State the preparation type.
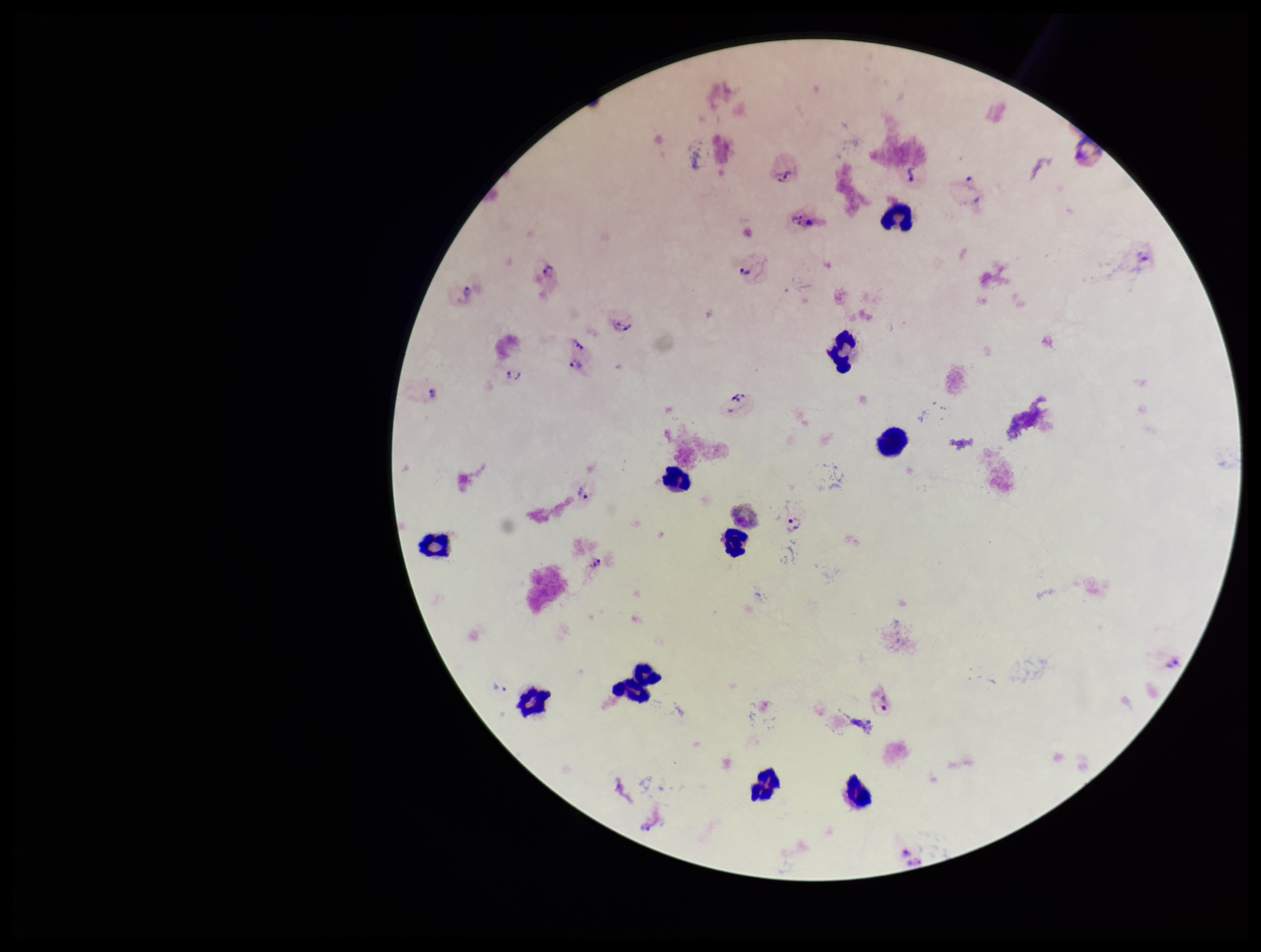
A thick smear.

Plasmodium parasites = seen
leukocyte count = 11
capture = smartphone photograph through the microscope eyepiece
species reported for this patient = Plasmodium vivax
stain = Giemsa
patient malaria status = positive
parasite count = 25
image size = 1261×952 pixels
field of view = single